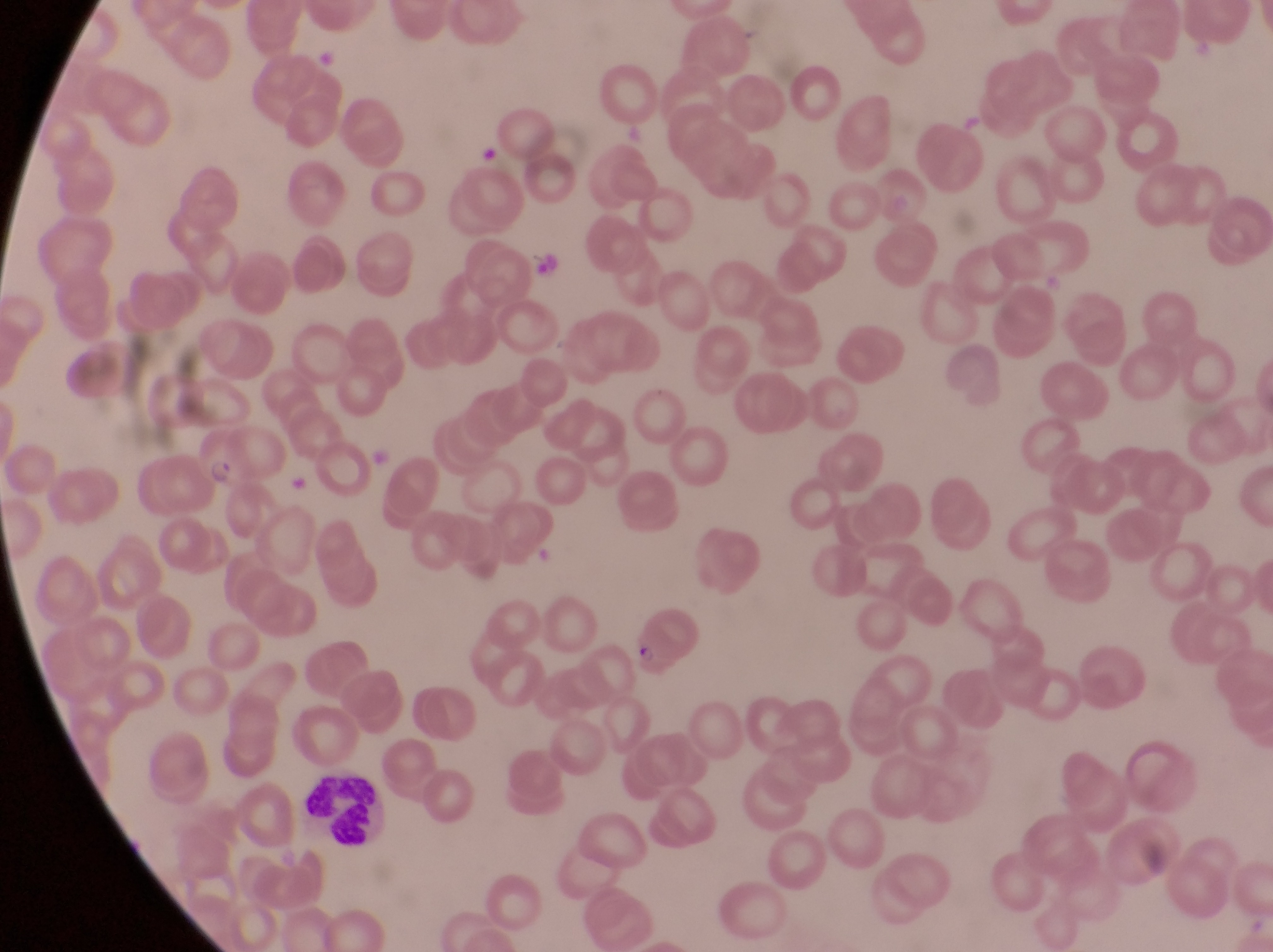

Approximate bounding boxes as {left, top, right, bottom} in pixels. Leukocyte locations: {305, 779, 380, 846}. Parasitised red blood cell locations: {187, 422, 252, 490}, {622, 602, 699, 672}. Photographed through the eyepiece of an Olympus CX-23 microscope with a smartphone camera. At a magnification of 1000x. Thin blood smear. Single field of view. Image is 1273×952 pixels. Collected in Uganda.